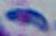
Summary:
  - Identification: Toxoplasma gondii
  - Magnification: 1000x
  - Modality: micrograph